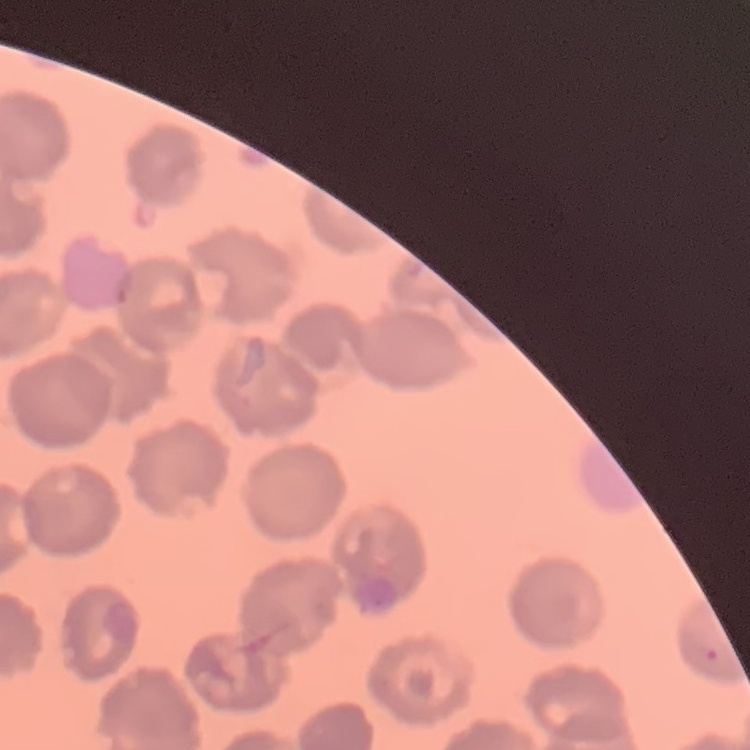

The red blood cells show no rouleaux formation. Thin peripheral smear. Stained with either Field's or Giemsa. Square crop of a larger photomicrograph.